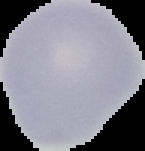
From a thin blood smear. Cell region segmented out of the field of view; the surrounding area is masked to black. Image is 145×151 pixels. Malaria status: uninfected.